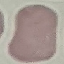 Malaria status: uninfected. Giemsa-stained preparation. Thin blood smear. Cell patch, automatically extracted from a larger field of view and resized to 64 × 64 pixels. Photographed with a smartphone camera at the microscope eyepiece.